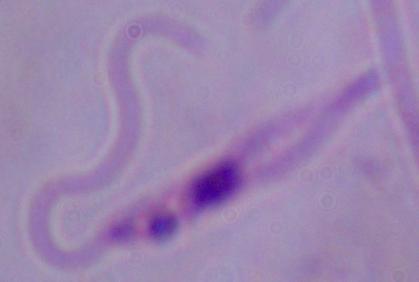 Photomicrograph. 1000x magnification. A Leishmania parasite is seen.